Comment on the morphology of the red blood cells.
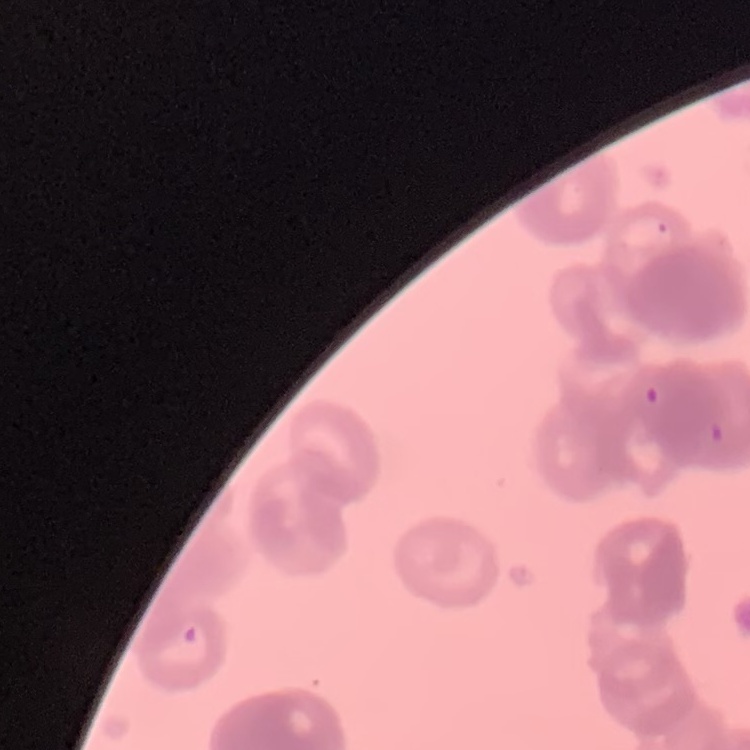
They show rouleaux formation.

One tile cut from a larger photomicrograph. Stained with either Field's or Giemsa. Thin blood smear.